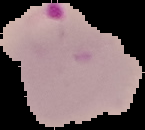 From a thin blood smear. Result: Plasmodium parasites detected. Image is 145×130 pixels. The area outside the segmented cell region is set to black.